Report the malaria status of this cell.
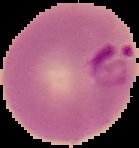
It is parasitized.

Summary:
  - Image type: cell region segmented out of the field of view; surrounding area masked to black
  - Image size: 139×148 pixels
  - Preparation: thin blood film